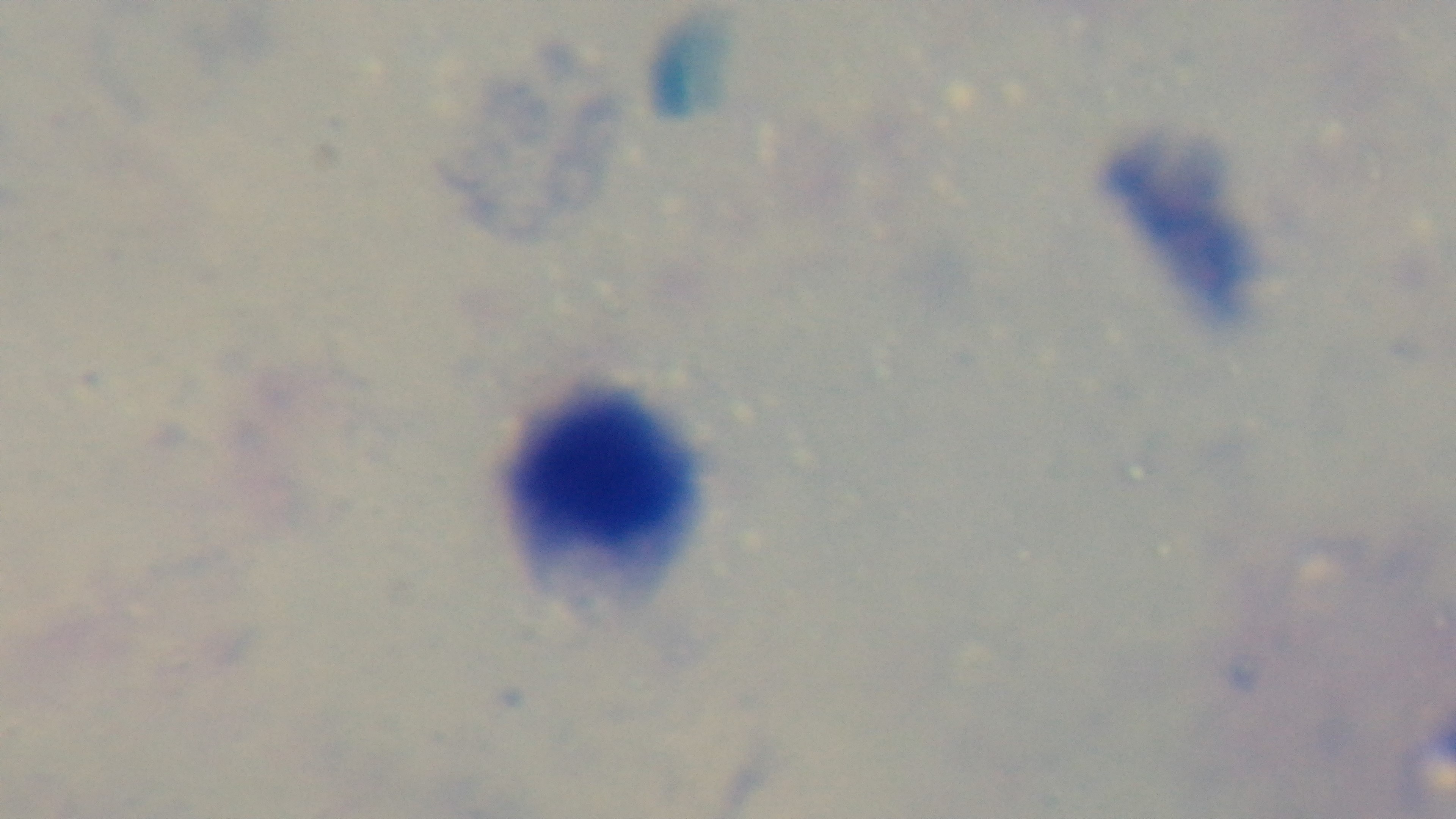

Summary:
  - Objective: 100x oil immersion
  - Modality: light microscopy
  - Capture: mounted 4K digital camera
  - Preparation: thick blood film
  - Field of view: single
  - Malaria status: negative
  - Stain: Giemsa